Outline each blood parasite and name the species.
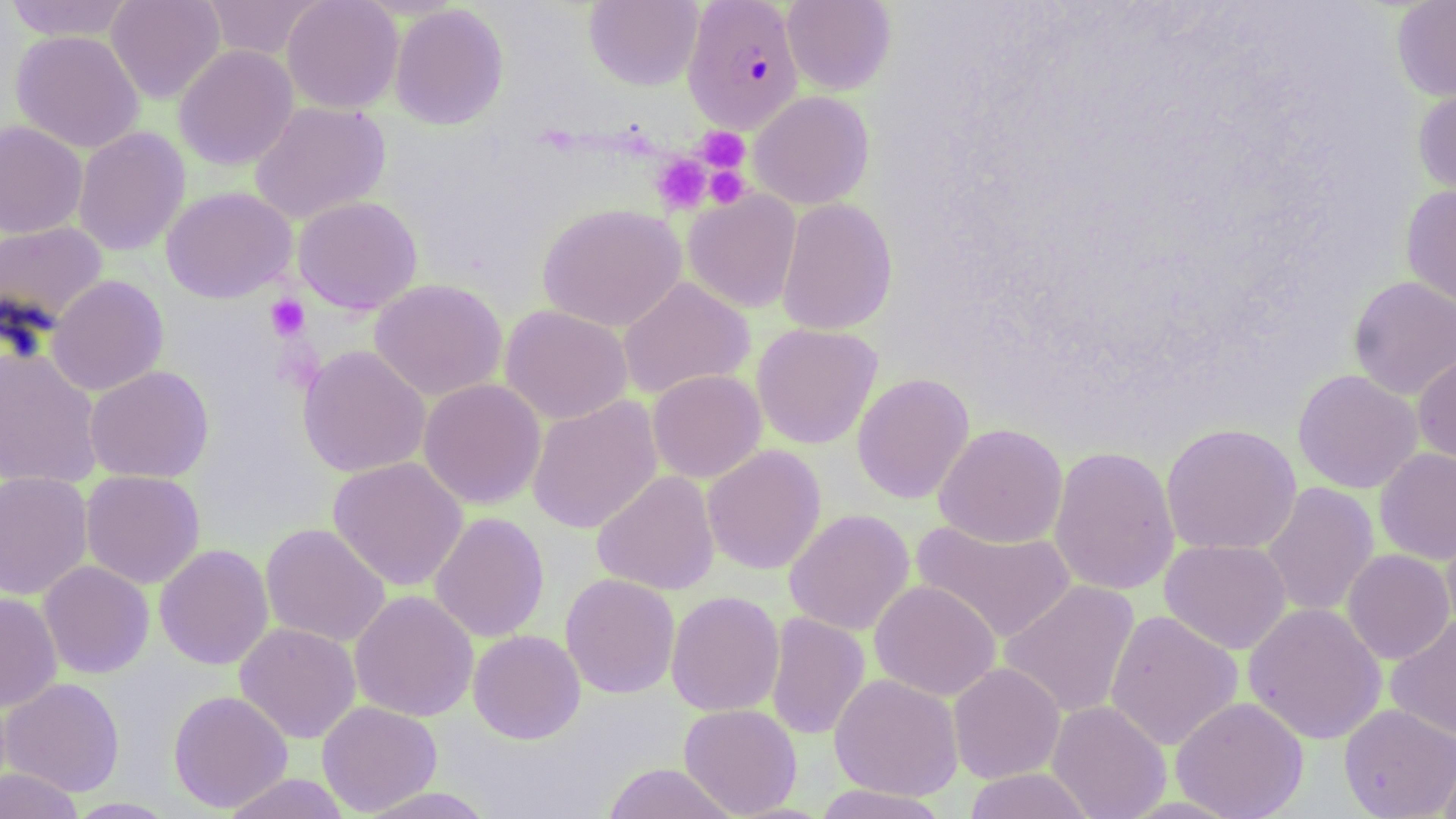
Approximate bounding boxes as named x1/y1/x2/y2 corners in pixels.
Plasmodium falciparum-infected red blood cells: (x1=683, y1=0, x2=804, y2=134).
No Plasmodium ovale, Plasmodium malariae, Plasmodium vivax, Babesia divergens, or Trypanosoma brucei observed.

Summary:
  - Platelet locations: (x1=699, y1=128, x2=750, y2=172), (x1=652, y1=154, x2=711, y2=213), (x1=704, y1=165, x2=751, y2=208), (x1=265, y1=295, x2=310, y2=341)
  - Uninfected red blood cell locations: (x1=3, y1=0, x2=137, y2=41), (x1=106, y1=0, x2=225, y2=104), (x1=200, y1=0, x2=326, y2=60), (x1=282, y1=0, x2=403, y2=113), (x1=584, y1=0, x2=703, y2=91), (x1=782, y1=0, x2=897, y2=95), (x1=1391, y1=0, x2=1456, y2=102), (x1=390, y1=4, x2=509, y2=131), (x1=10, y1=30, x2=144, y2=153), (x1=174, y1=45, x2=298, y2=170), (x1=1412, y1=83, x2=1456, y2=206), (x1=749, y1=91, x2=874, y2=209), (x1=250, y1=101, x2=391, y2=225), (x1=0, y1=121, x2=87, y2=238), (x1=73, y1=126, x2=190, y2=257), (x1=1400, y1=185, x2=1456, y2=313), (x1=161, y1=186, x2=297, y2=303), (x1=683, y1=190, x2=802, y2=313), (x1=293, y1=196, x2=423, y2=314), (x1=775, y1=198, x2=897, y2=335), (x1=537, y1=203, x2=687, y2=332), (x1=0, y1=221, x2=109, y2=333), (x1=47, y1=275, x2=169, y2=395), (x1=1347, y1=275, x2=1456, y2=401), (x1=617, y1=277, x2=755, y2=400), (x1=369, y1=278, x2=508, y2=401), (x1=500, y1=304, x2=633, y2=424), (x1=751, y1=323, x2=883, y2=450), (x1=297, y1=345, x2=431, y2=478), (x1=0, y1=346, x2=102, y2=488), (x1=1413, y1=351, x2=1456, y2=468), (x1=85, y1=365, x2=214, y2=483), (x1=647, y1=369, x2=766, y2=483), (x1=1292, y1=369, x2=1423, y2=493), (x1=852, y1=372, x2=975, y2=504), (x1=418, y1=378, x2=546, y2=510), (x1=527, y1=396, x2=663, y2=534), (x1=933, y1=423, x2=1068, y2=548), (x1=1161, y1=423, x2=1301, y2=555), (x1=702, y1=445, x2=826, y2=574), (x1=1048, y1=445, x2=1180, y2=596), (x1=1375, y1=448, x2=1456, y2=565), (x1=328, y1=456, x2=468, y2=591), (x1=81, y1=470, x2=205, y2=588), (x1=591, y1=470, x2=720, y2=595), (x1=0, y1=471, x2=93, y2=600), (x1=1261, y1=482, x2=1380, y2=618), (x1=784, y1=509, x2=915, y2=635), (x1=429, y1=512, x2=549, y2=642), (x1=910, y1=519, x2=1077, y2=643), (x1=1441, y1=522, x2=1456, y2=639), (x1=260, y1=523, x2=390, y2=647), (x1=1160, y1=539, x2=1292, y2=654), (x1=154, y1=544, x2=274, y2=670), (x1=1341, y1=549, x2=1454, y2=664), (x1=38, y1=560, x2=155, y2=679), (x1=560, y1=573, x2=681, y2=699), (x1=869, y1=580, x2=1001, y2=701), (x1=999, y1=580, x2=1141, y2=719), (x1=350, y1=590, x2=479, y2=722), (x1=666, y1=590, x2=784, y2=717), (x1=0, y1=592, x2=62, y2=711), (x1=1243, y1=602, x2=1387, y2=745), (x1=1105, y1=610, x2=1243, y2=751), (x1=765, y1=612, x2=870, y2=740), (x1=1385, y1=616, x2=1456, y2=743), (x1=234, y1=622, x2=361, y2=744), (x1=468, y1=629, x2=586, y2=744), (x1=948, y1=662, x2=1065, y2=784), (x1=829, y1=673, x2=963, y2=801), (x1=1, y1=677, x2=125, y2=797), (x1=168, y1=690, x2=293, y2=813), (x1=1171, y1=696, x2=1309, y2=819), (x1=316, y1=700, x2=443, y2=816), (x1=1046, y1=700, x2=1171, y2=819), (x1=679, y1=703, x2=803, y2=817), (x1=1339, y1=703, x2=1456, y2=818), (x1=1438, y1=743, x2=1456, y2=819), (x1=601, y1=763, x2=739, y2=819), (x1=0, y1=767, x2=84, y2=819), (x1=963, y1=768, x2=1096, y2=819), (x1=222, y1=773, x2=351, y2=818), (x1=811, y1=784, x2=950, y2=818), (x1=354, y1=786, x2=498, y2=819), (x1=64, y1=797, x2=179, y2=818)
  - Slide-level diagnosis: Plasmodium falciparum
  - Image size: 1456×819 pixels
  - Stain: May-Grünwald-Giemsa
  - Modality: light microscopy
  - Preparation: thin blood film
  - Magnification: 1000x
  - Field of view: single